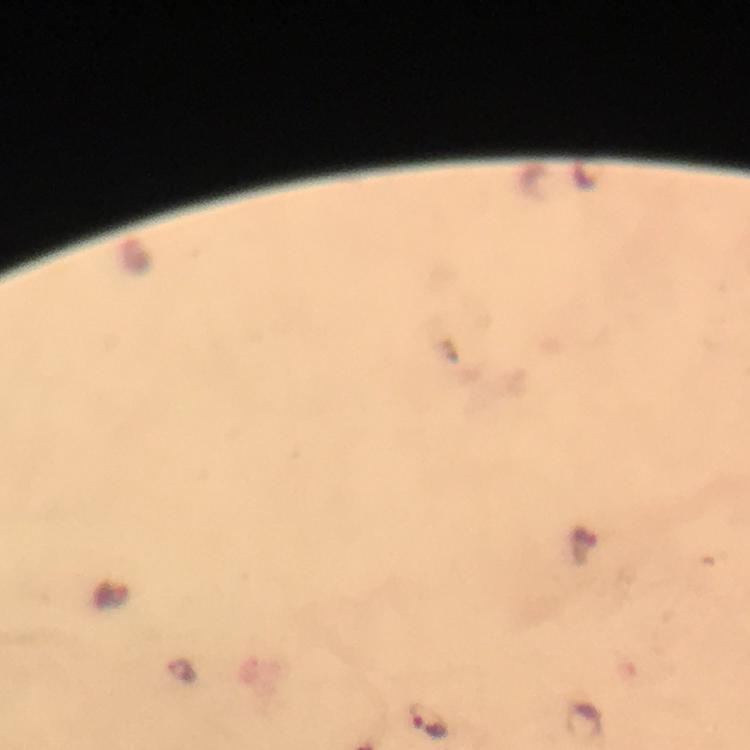

Approximate object centers, in pixels from the top-left corner.
Summary:
  - Malaria parasite locations: (x=183, y=671), (x=427, y=720)
  - Image size: 750×750 pixels
  - Capture: smartphone mounted on the microscope
  - Magnification: 100x
  - Immersion oil: used
  - Cropped from: one field of view
  - Stain: Giemsa
  - Context: from a malaria diagnostic workup
  - Preparation: thick blood film